Locate platelets.
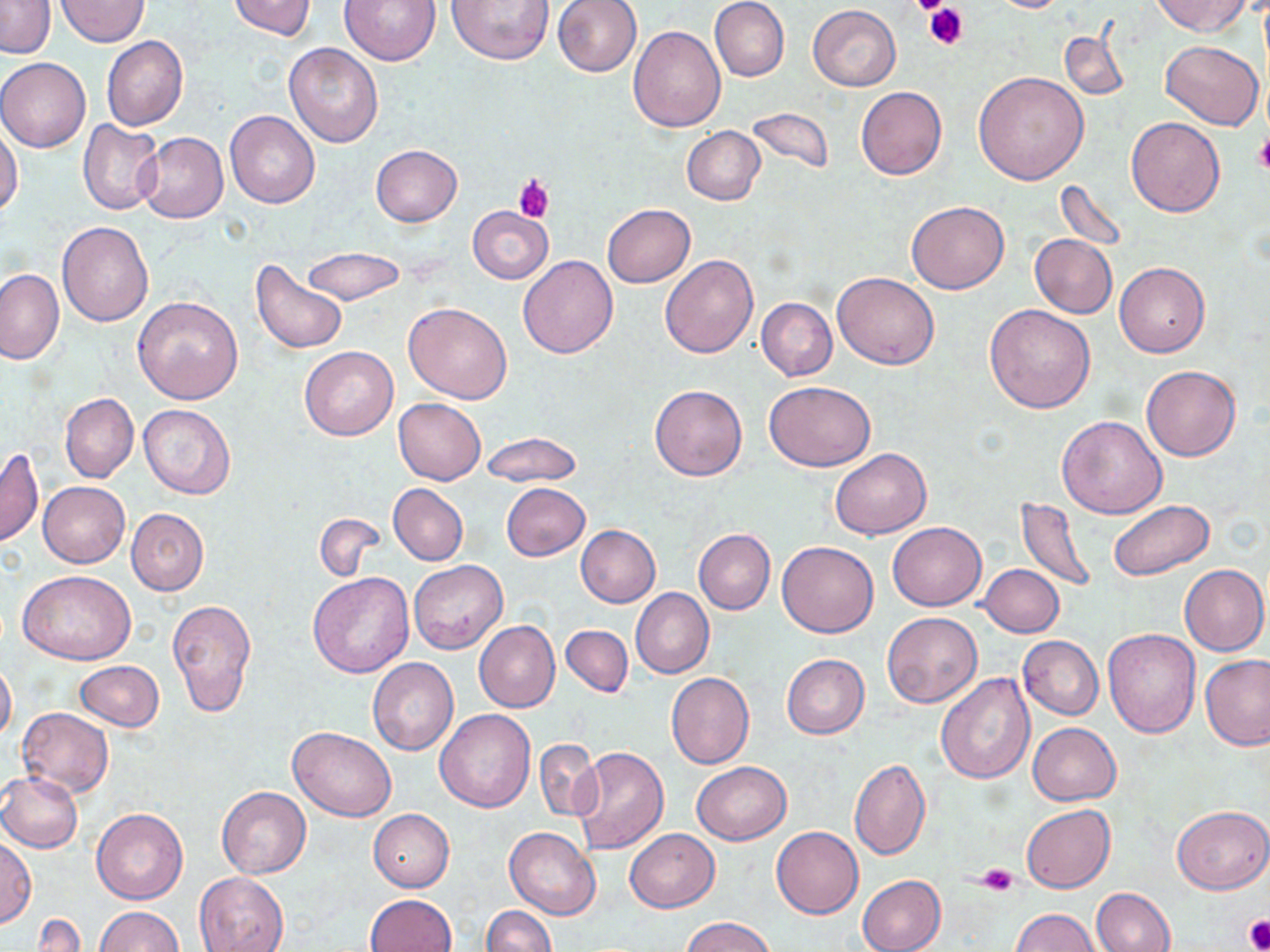
Approximate bounding boxes as (x1,y1)-(x2,y2) corner pairs in pixels.
Platelets: (906,0)-(954,17), (923,3)-(969,51), (1254,136)-(1270,174), (513,177)-(556,224), (977,863)-(1019,895), (1244,915)-(1270,952).

Summary:
  - Uninfected red blood cell locations: (55,0)-(150,46), (228,0)-(316,40), (337,0)-(443,66), (446,0)-(555,65), (552,0)-(642,76), (710,0)-(790,82), (988,0)-(1071,13), (1154,0)-(1252,37), (0,1)-(55,59), (807,5)-(901,90), (628,25)-(725,130), (1058,31)-(1130,103), (102,36)-(188,130), (1162,39)-(1263,129), (284,43)-(383,147), (0,57)-(91,152), (974,71)-(1089,184), (856,86)-(947,179), (749,107)-(834,175), (225,110)-(320,208), (1126,117)-(1224,217), (78,119)-(165,216), (682,125)-(765,206), (0,126)-(24,220), (137,132)-(228,223), (371,145)-(462,226), (1054,179)-(1130,253), (906,202)-(1009,294), (602,204)-(695,288), (468,206)-(553,283), (57,222)-(153,326), (1030,234)-(1116,317), (302,247)-(406,305), (518,255)-(618,358), (660,255)-(758,358), (251,260)-(348,355), (1115,263)-(1210,358), (0,270)-(63,365), (832,271)-(940,370), (132,296)-(244,405), (756,297)-(837,380), (404,302)-(513,404), (984,304)-(1097,413), (299,346)-(398,440), (1141,365)-(1240,461), (764,381)-(877,470), (650,384)-(747,481), (60,393)-(138,483), (394,398)-(486,484), (138,404)-(236,500), (1059,415)-(1166,518), (480,432)-(581,486), (0,447)-(43,548), (831,448)-(931,539), (38,481)-(129,567), (388,483)-(468,565), (500,483)-(589,561), (1014,496)-(1098,592), (1107,499)-(1215,580), (126,508)-(209,596), (314,513)-(385,581), (887,522)-(987,610), (576,526)-(660,608), (693,528)-(775,614), (776,541)-(878,637), (408,559)-(508,654), (980,563)-(1063,637), (1180,564)-(1268,655), (18,569)-(135,664), (308,572)-(413,677), (630,588)-(714,678), (166,598)-(256,717), (883,612)-(982,708), (474,621)-(560,713), (560,625)-(633,696), (1102,629)-(1201,738), (1017,637)-(1103,720), (1200,653)-(1270,750), (781,654)-(870,739), (368,657)-(459,755), (0,660)-(16,742), (75,660)-(164,730), (666,672)-(754,769), (934,672)-(1035,784), (17,707)-(113,797), (434,709)-(536,812), (1027,722)-(1123,806), (288,726)-(397,821), (534,739)-(602,822), (571,746)-(670,853), (849,759)-(931,860), (691,760)-(792,844), (0,771)-(83,852), (216,785)-(311,878), (1021,805)-(1115,893), (1171,806)-(1269,895), (91,808)-(187,904), (368,809)-(454,891), (503,826)-(601,921), (771,826)-(864,919), (624,829)-(719,911), (0,836)-(35,925), (194,872)-(289,952), (857,875)-(946,952), (1090,887)-(1175,952), (364,894)-(456,952), (96,906)-(182,952), (482,906)-(556,952), (1010,908)-(1098,952), (681,916)-(775,952), (33,917)-(85,951)
  - Slide-level diagnosis: negative for blood parasites
  - Image size: 1270×952 pixels
  - Stain: May-Grünwald-Giemsa
  - Field of view: single
  - Preparation: thin blood film
  - Magnification: 1000x
  - Modality: light microscopy